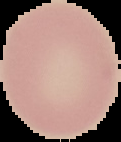
Summary:
  - Preparation: thin blood film
  - Result: no Plasmodium parasites detected
  - Image type: segmented cell region on a black background
  - Image size: 121×142 pixels